Outline each blood parasite and name the species.
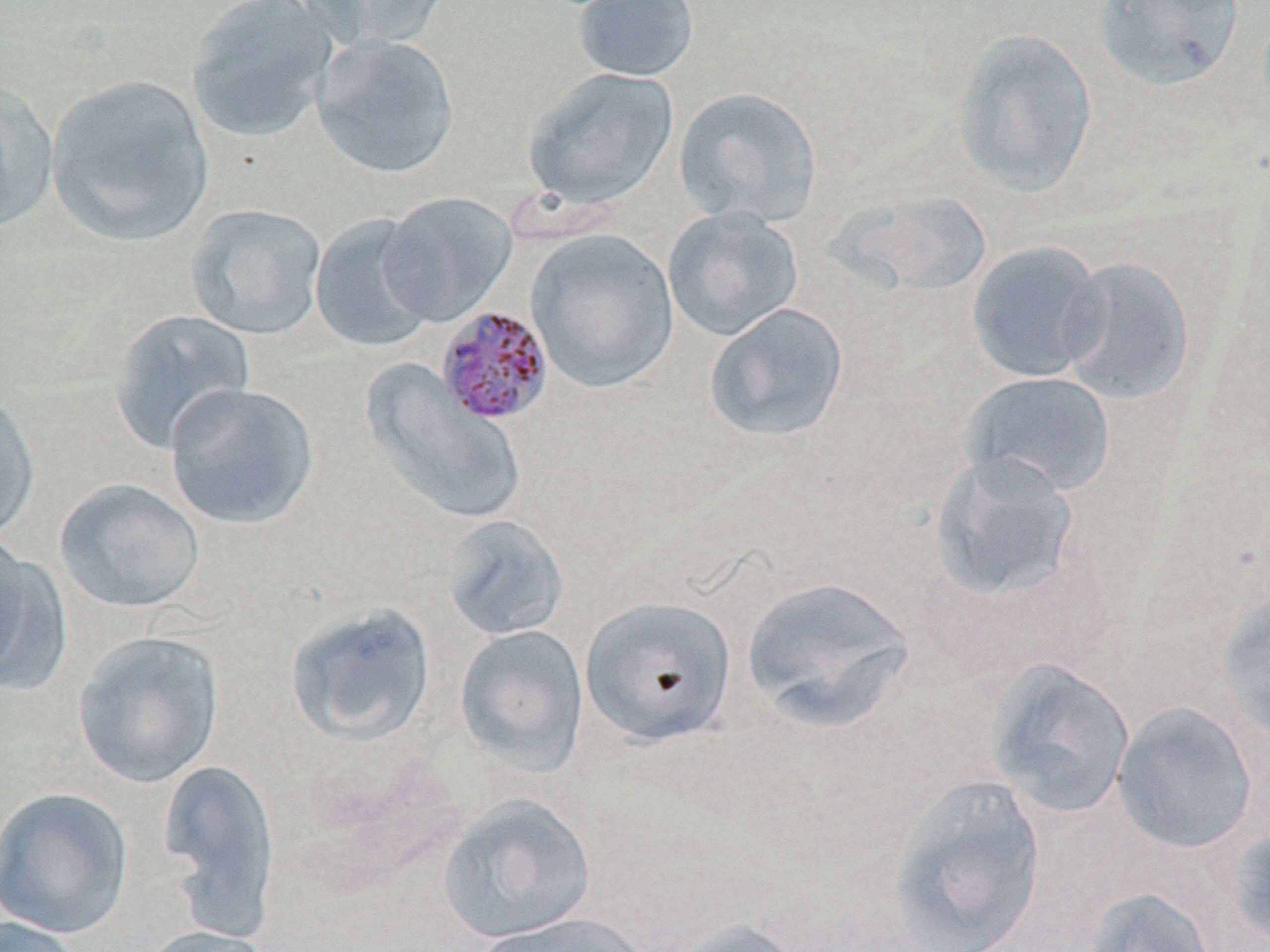
Approximate bounding boxes as (x1,y1)-(x2,y2) corner pairs in pixels.
Plasmodium malariae-infected red blood cells: (435,306)-(553,425).
No Plasmodium falciparum, Plasmodium ovale, Plasmodium vivax, Babesia divergens, or Trypanosoma brucei observed.

{
  "slide_level_diagnosis": "Plasmodium malariae",
  "image_size": "1270×952 pixels",
  "uninfected_red_blood_cell_locations": "approximate bounding boxes as (x1,y1)-(x2,y2) corner pairs in pixels: (185,0)-(339,143), (297,0)-(453,53), (569,0)-(700,83), (1092,0)-(1244,90), (951,29)-(1098,198), (311,35)-(460,179), (522,67)-(679,210), (45,73)-(215,247), (0,81)-(59,235), (674,86)-(823,228), (830,190)-(993,299), (378,191)-(517,327), (185,204)-(327,340), (663,206)-(804,342), (309,214)-(438,353), (525,227)-(679,394), (966,240)-(1108,383), (1057,255)-(1195,405), (704,302)-(850,443), (107,309)-(255,454), (364,363)-(526,526), (959,371)-(1116,498), (164,382)-(320,530), (0,390)-(40,545), (929,451)-(1081,603), (54,478)-(205,615), (441,514)-(569,641), (0,534)-(65,692), (741,575)-(919,731), (1214,590)-(1270,744), (580,595)-(738,746), (284,602)-(436,746), (454,624)-(590,776), (72,630)-(224,788), (983,656)-(1137,819), (1112,701)-(1258,854), (157,757)-(283,939), (885,774)-(1048,952), (0,786)-(133,939), (437,794)-(596,943), (1229,823)-(1270,950), (1082,885)-(1217,952), (467,911)-(660,952), (0,916)-(87,952), (660,917)-(807,952), (136,925)-(278,952)",
  "preparation": "thin blood smear",
  "field_of_view": "single",
  "stain": "May-Grünwald-Giemsa",
  "modality": "light microscopy",
  "magnification": "1000x"
}